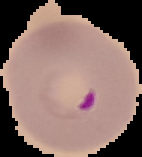
image_type: segmented cell region with the area outside set to black
result: malaria parasites detected
preparation: thin blood film
image_size: 142×157 pixels